Outline each uninfected red blood cell.
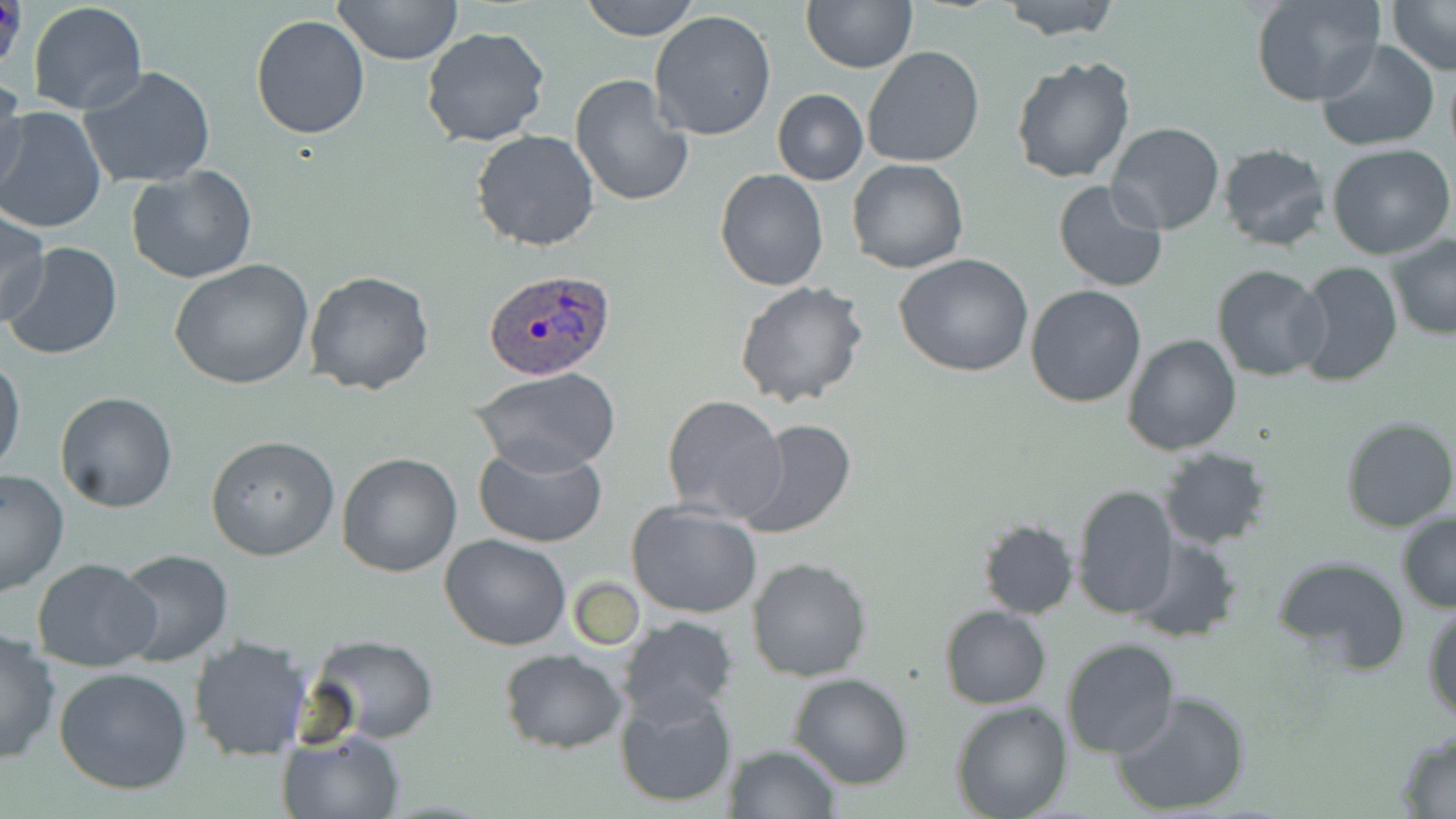

Approximate bounding boxes as (x1, y1, x2, y2) in pixels.
Uninfected red blood cells: (333, 0, 461, 66), (578, 0, 702, 42), (801, 0, 918, 72), (997, 0, 1123, 41), (1251, 0, 1386, 106), (1384, 0, 1455, 74), (26, 2, 148, 116), (649, 9, 779, 141), (250, 13, 373, 140), (421, 27, 551, 148), (1317, 39, 1438, 151), (863, 45, 984, 168), (1011, 57, 1135, 184), (80, 67, 218, 189), (569, 74, 694, 209), (0, 75, 29, 199), (772, 88, 868, 185), (0, 107, 106, 233), (1108, 122, 1225, 235), (470, 130, 601, 252), (1326, 142, 1455, 260), (1217, 143, 1330, 252), (847, 159, 968, 274), (126, 165, 258, 283), (714, 170, 829, 292), (1053, 180, 1171, 292), (0, 207, 50, 328), (1386, 234, 1456, 341), (4, 242, 123, 363), (895, 253, 1033, 377), (169, 260, 315, 391), (1295, 260, 1403, 389), (1211, 264, 1329, 381), (304, 271, 435, 394), (735, 282, 869, 409), (1026, 284, 1146, 407), (1122, 334, 1242, 457), (0, 354, 26, 479), (470, 368, 622, 478), (55, 391, 180, 513), (661, 394, 787, 525), (1341, 416, 1456, 533), (736, 418, 857, 540), (206, 434, 339, 560), (473, 443, 609, 549), (1156, 446, 1273, 550), (335, 453, 463, 577), (0, 470, 70, 597), (1070, 484, 1177, 620), (627, 501, 763, 618), (1396, 511, 1456, 612), (978, 519, 1078, 618), (1128, 531, 1241, 642), (440, 534, 571, 651), (114, 548, 234, 665), (1271, 555, 1410, 676), (31, 558, 161, 671), (747, 558, 872, 681), (567, 578, 646, 649), (1423, 602, 1456, 724), (941, 605, 1051, 709), (619, 616, 741, 725), (0, 628, 61, 766), (187, 635, 311, 760), (310, 636, 438, 743), (1062, 637, 1180, 758), (498, 647, 628, 753), (54, 667, 192, 795), (789, 673, 912, 790), (613, 683, 738, 808), (1112, 689, 1252, 816), (952, 701, 1072, 819), (279, 730, 405, 819), (1395, 731, 1456, 817), (724, 744, 840, 819).

Summary:
  - Plasmodium ovale-infected red blood cell locations: (481, 268, 617, 381)
  - Slide-level diagnosis: Plasmodium ovale
  - Magnification: 1000x
  - Image size: 1456×819 pixels
  - Stain: May-Grünwald-Giemsa
  - Field of view: one of a larger specimen
  - Preparation: thin blood film
  - Modality: optical microscopy